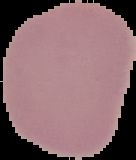
Summary:
  - Malaria status: uninfected
  - Image size: 136×160 pixels
  - Preparation: thin blood smear
  - Image type: segmented cell region with the area outside set to black